Comment on the morphology of the red blood cells.
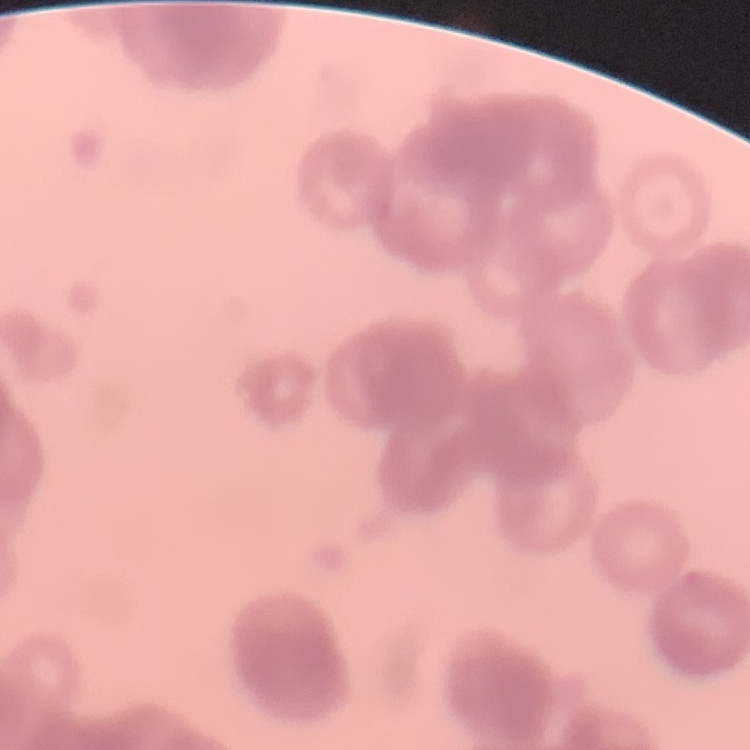
Rouleaux formation.

Thin blood smear. Square crop of a larger photomicrograph. Field's or Giemsa stain.